Give the position of every leukocyte visible.
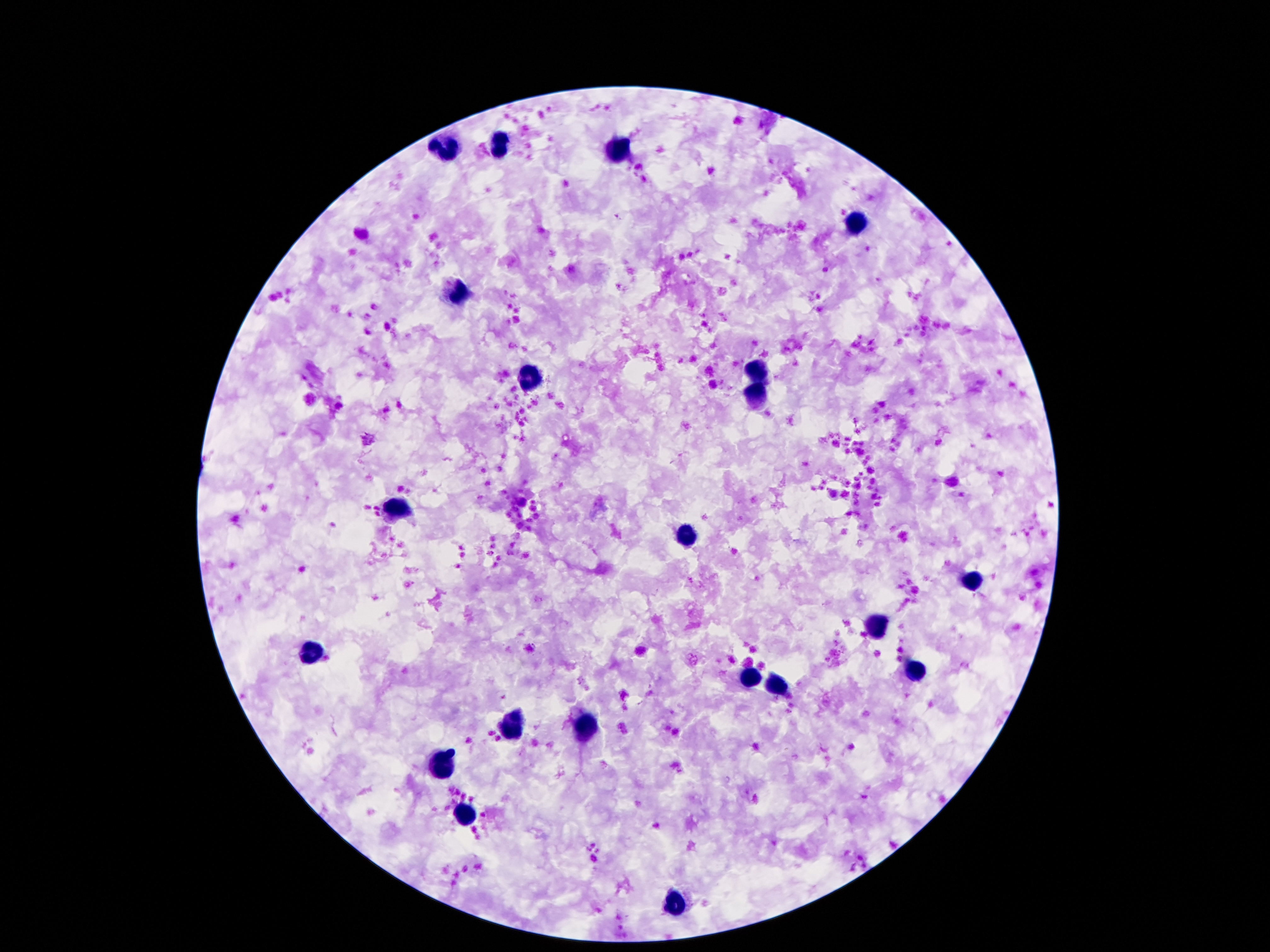

Approximate centers as [x, y] in pixels.
Leukocytes: [502, 145], [448, 147], [614, 152], [854, 221], [459, 292], [757, 372], [530, 376], [756, 397], [399, 509], [686, 535], [973, 580], [879, 625], [313, 652], [914, 670], [749, 676], [778, 685], [513, 722], [588, 725], [445, 766], [467, 815], [672, 906].

Thick blood smear. Giemsa stain. Patient malaria status: not infected. Single field of view. Image is 1270×952 pixels. 100x magnification. Smartphone photograph taken through the microscope eyepiece.